Give the extent of all Plasmodium falciparum-infected red blood cells.
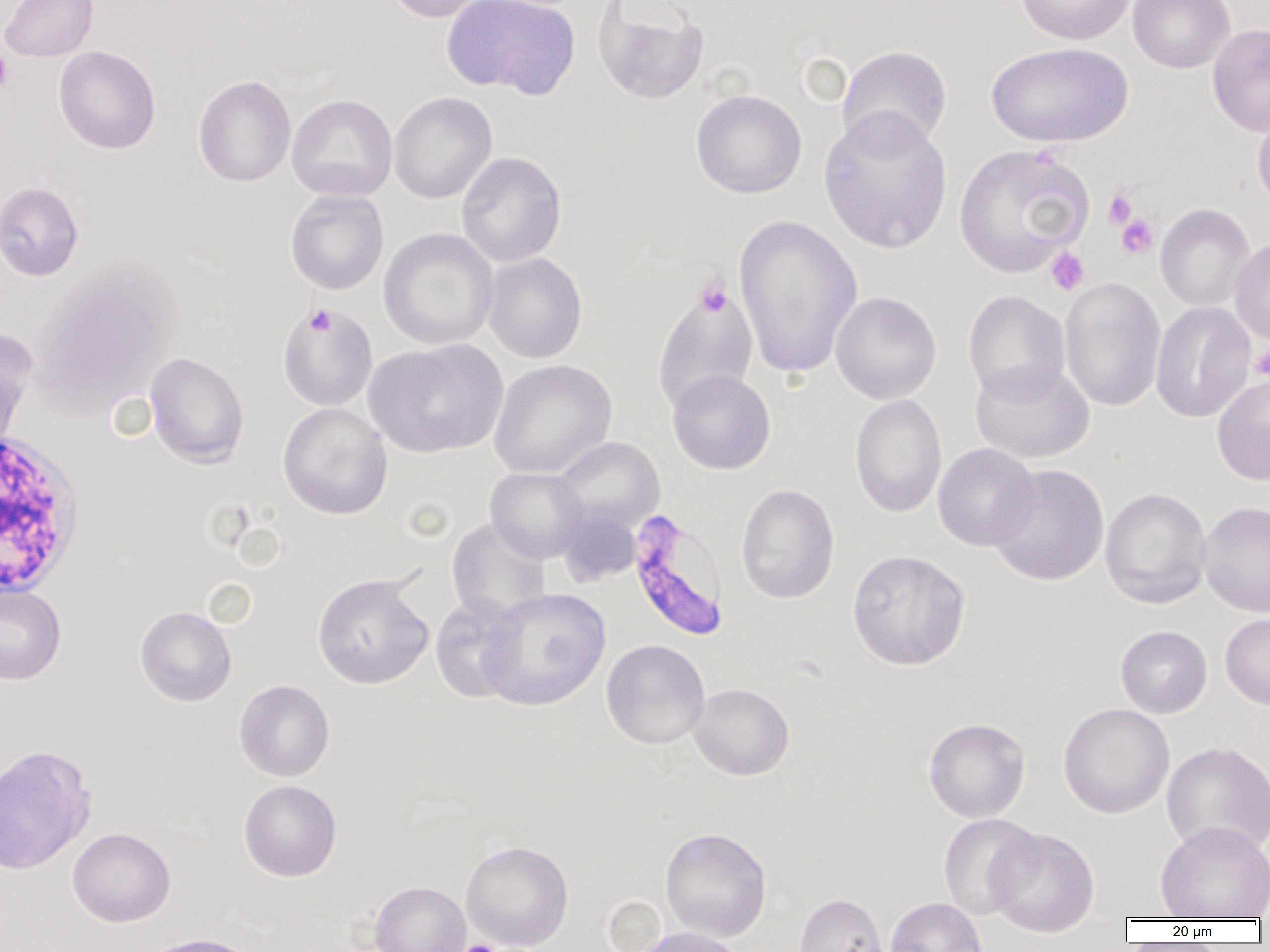
Approximate bounding boxes as [x1, y1, x2, y2] in pixels.
Plasmodium falciparum-infected red blood cells: [627, 509, 730, 642].

slide_level_diagnosis: Plasmodium falciparum
preparation: thin blood film
magnification: 1000x
platelet_locations: 'approximate bounding boxes as [x1, y1, x2, y2] in pixels: [0, 48, 13, 95], [1103, 188, 1137, 229], [1115, 213, 1159, 260], [1045, 247, 1090, 295], [695, 278, 732, 317], [305, 305, 336, 337], [1249, 344, 1270, 381], [454, 939, 502, 952]'
white_blood_cell_locations: 'approximate bounding boxes as [x1, y1, x2, y2] in pixels: [1, 432, 86, 598]'
uninfected_red_blood_cell_locations: 'approximate bounding boxes as [x1, y1, x2, y2] in pixels: [0, 0, 99, 61], [384, 0, 496, 23], [441, 0, 580, 99], [591, 0, 710, 105], [1015, 0, 1136, 45], [1127, 0, 1235, 73], [1207, 23, 1270, 137], [987, 41, 1133, 148], [53, 45, 161, 154], [837, 45, 952, 153], [193, 74, 296, 187], [691, 89, 807, 199], [389, 92, 497, 204], [286, 94, 397, 201], [818, 108, 952, 253], [1252, 108, 1270, 216], [954, 144, 1094, 275], [456, 151, 566, 267], [0, 181, 84, 281], [285, 190, 388, 294], [1155, 203, 1255, 312], [732, 213, 863, 379], [378, 228, 499, 350], [1230, 237, 1270, 346], [483, 252, 587, 363], [29, 256, 181, 411], [1058, 277, 1166, 412], [652, 285, 758, 413], [963, 290, 1070, 402], [830, 291, 942, 404], [1150, 301, 1256, 423], [277, 304, 378, 411], [0, 328, 37, 447], [365, 340, 507, 458], [145, 352, 249, 468], [489, 359, 616, 479], [970, 360, 1094, 463], [667, 370, 776, 474], [1212, 373, 1270, 486], [850, 393, 946, 517], [277, 401, 393, 519], [551, 437, 665, 533], [933, 443, 1040, 551], [987, 464, 1110, 585], [485, 467, 589, 563], [736, 483, 839, 604], [1100, 487, 1212, 608], [1199, 501, 1270, 618], [556, 505, 642, 586], [447, 518, 551, 625], [847, 549, 971, 671], [312, 573, 433, 689], [0, 583, 66, 685], [478, 588, 610, 711], [430, 595, 525, 703], [135, 605, 236, 706], [1220, 613, 1270, 711], [1115, 625, 1213, 718], [601, 639, 710, 749], [234, 679, 335, 782], [688, 683, 794, 780], [1057, 702, 1175, 819], [923, 717, 1030, 822], [1161, 740, 1270, 857], [0, 744, 96, 876], [238, 780, 342, 882], [937, 814, 1042, 919], [1155, 820, 1270, 920], [660, 826, 772, 942], [986, 826, 1100, 937], [67, 827, 176, 927], [460, 839, 573, 950], [369, 873, 573, 950], [369, 881, 470, 952], [793, 892, 890, 952], [885, 897, 986, 952], [633, 927, 745, 952], [137, 933, 263, 952]'
field_of_view: single
image_size: 1270×952 pixels
modality: light microscopy